Assess this cell for malaria.
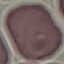

Uninfected.

Summary:
  - Preparation: thin blood film
  - Capture: smartphone through the microscope eyepiece
  - Image type: cell patch, automatically extracted from a larger field of view and resized to 64 × 64 pixels
  - Stain: Giemsa